Report the malaria status of this cell.
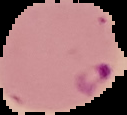
It is parasitized.

image_size: 127×115 pixels
preparation: thin blood smear
image_type: cell region segmented out of the field of view; surrounding area masked to black